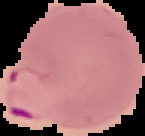

image_type: segmented cell region on a black background
image_size: 145×136 pixels
preparation: thin blood smear
result: malaria parasites detected